State which parasite is depicted.
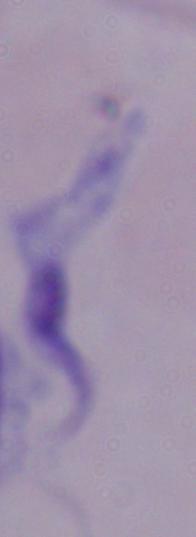
A trypanosome.

magnification = 1000x
modality = micrograph